Describe the morphology of the erythrocytes.
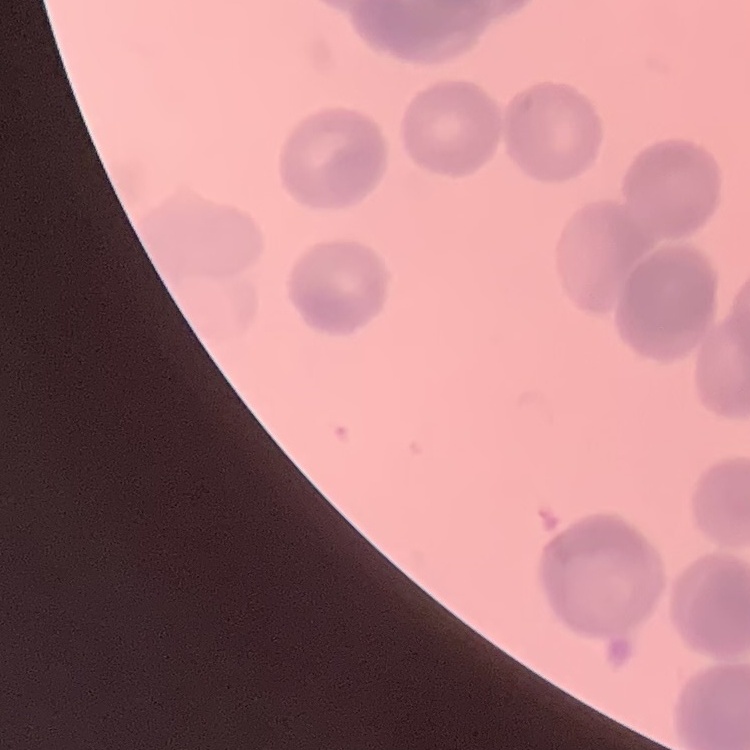
Rouleaux formation.

image type = one tile cut from a larger photomicrograph
stain = Field's or Giemsa
preparation = thin peripheral smear